Comment on the morphology of the red blood cells.
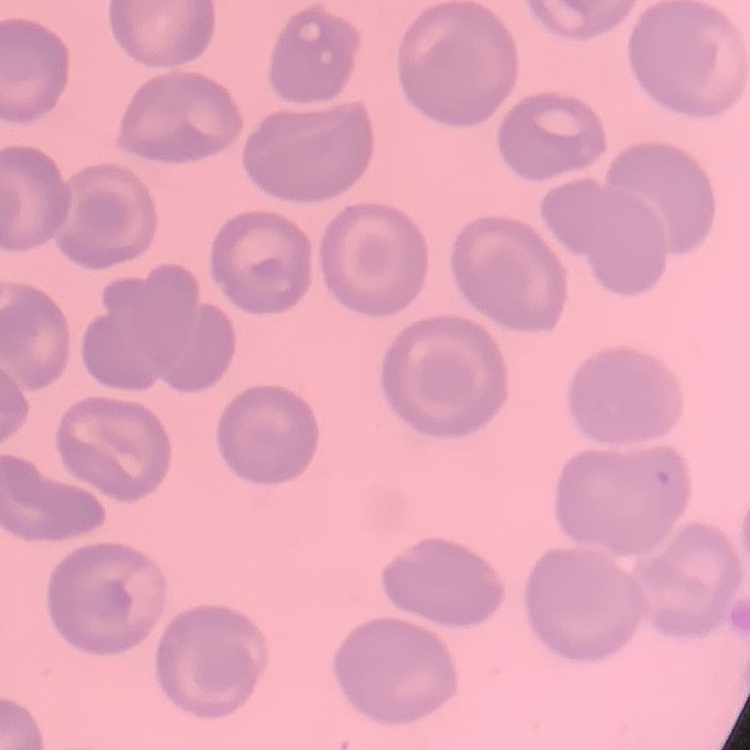
No rouleaux formation.

Summary:
  - Preparation: thin blood smear
  - Stain: Field's or Giemsa
  - Image type: one tile cut from a larger photomicrograph